Find each parasitized red blood cell.
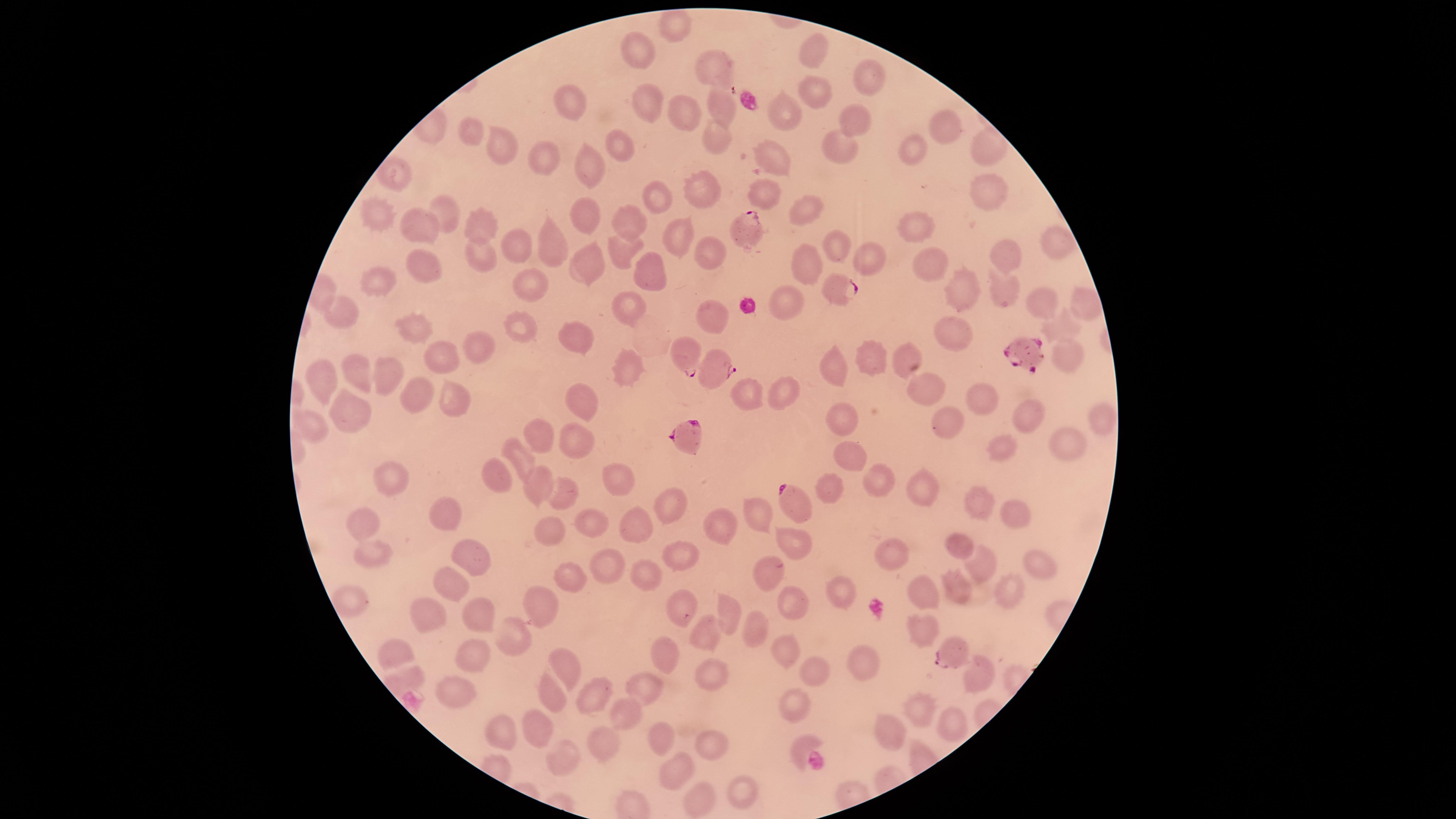
Approximate marker points as (x, y) in pixels.
Parasitized red blood cells: (748, 228), (837, 283), (1019, 350), (686, 358), (715, 369), (684, 434), (785, 498), (953, 653).

Approximate marker points as (x, y) in pixels.
Summary:
  - Uninfected red blood cells: (671, 28), (642, 48), (812, 52), (715, 69), (868, 74), (809, 94), (646, 102), (572, 104), (720, 112), (683, 115), (783, 115), (854, 123), (946, 125), (472, 131), (980, 141), (619, 142), (715, 142), (499, 143), (842, 148), (773, 153), (912, 153), (592, 163), (545, 164), (390, 173), (701, 193), (764, 195), (994, 197), (653, 200), (444, 210), (808, 211), (576, 214), (374, 219), (631, 222), (486, 227), (907, 228), (416, 229), (679, 233), (549, 241), (513, 243), (1059, 243), (837, 246), (618, 249), (707, 254), (1003, 256), (482, 261), (807, 261), (866, 261), (936, 263), (591, 264), (427, 267), (652, 271), (378, 283), (531, 286), (1000, 286), (961, 293), (1038, 300), (784, 302), (633, 303), (1083, 307), (344, 313), (713, 318), (410, 327), (522, 329), (1059, 332), (946, 333), (572, 334), (477, 344), (437, 354), (901, 355), (1072, 356), (877, 366), (838, 369), (629, 372), (356, 374), (385, 376), (319, 379), (922, 383), (982, 391), (417, 393), (580, 393), (740, 397), (449, 398), (784, 399), (1032, 409), (345, 412), (944, 421), (843, 422), (1101, 422), (307, 424), (541, 435), (578, 439), (1066, 442), (1001, 449), (850, 455), (522, 456), (489, 476), (388, 477), (620, 479), (882, 481), (918, 485), (535, 488), (560, 495), (830, 499), (979, 499), (671, 503), (754, 509), (447, 515), (1010, 515), (364, 520), (716, 521), (587, 525), (637, 527), (546, 529), (793, 542), (962, 547), (371, 552), (681, 553), (475, 554), (1038, 559), (891, 564), (610, 567), (982, 567), (644, 569), (762, 569), (575, 572), (452, 579), (917, 591), (840, 592), (957, 592), (1004, 592), (787, 597), (349, 599), (681, 600), (547, 609), (432, 611), (724, 613), (483, 615), (751, 629), (922, 630), (514, 636), (705, 636), (785, 646), (667, 653), (474, 654), (400, 657), (865, 663), (574, 666), (712, 674), (816, 674), (977, 674), (650, 683), (454, 696), (553, 697), (796, 709), (923, 712), (626, 715), (957, 719), (537, 725), (894, 735), (653, 737), (500, 742), (803, 742), (603, 747), (705, 750), (559, 755), (675, 774), (740, 797), (697, 803)
  - Capture: smartphone photograph through the microscope eyepiece
  - Preparation: thin blood film
  - Visible region: circular
  - Field of view: single
  - Species: Plasmodium falciparum
  - Image size: 1456×819 pixels
  - Stain: Giemsa